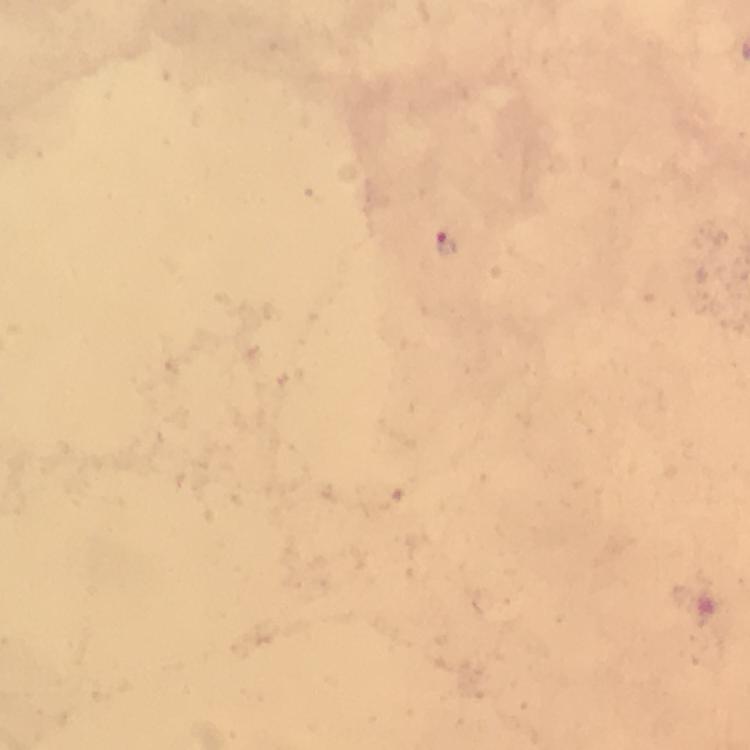
Approximate object centers, in pixels from the top-left corner.
Summary:
  - Plasmodium parasite locations: (x=445, y=244)
  - Magnification: 100x
  - Cropped from: a single field of view
  - Capture: smartphone camera through the microscope
  - Stain: Giemsa
  - Image size: 750×750 pixels
  - Immersion oil: used
  - Context: from a diagnostic examination for malaria
  - Preparation: thick blood film